Assess this cell for malaria.
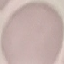

It is uninfected.

Cell patch, automatically extracted from a larger field of view and resized to 64 × 64 pixels. Photographed with a smartphone camera at the microscope eyepiece. Giemsa stain. Thin smear of blood.